Locate every Plasmodium parasite.
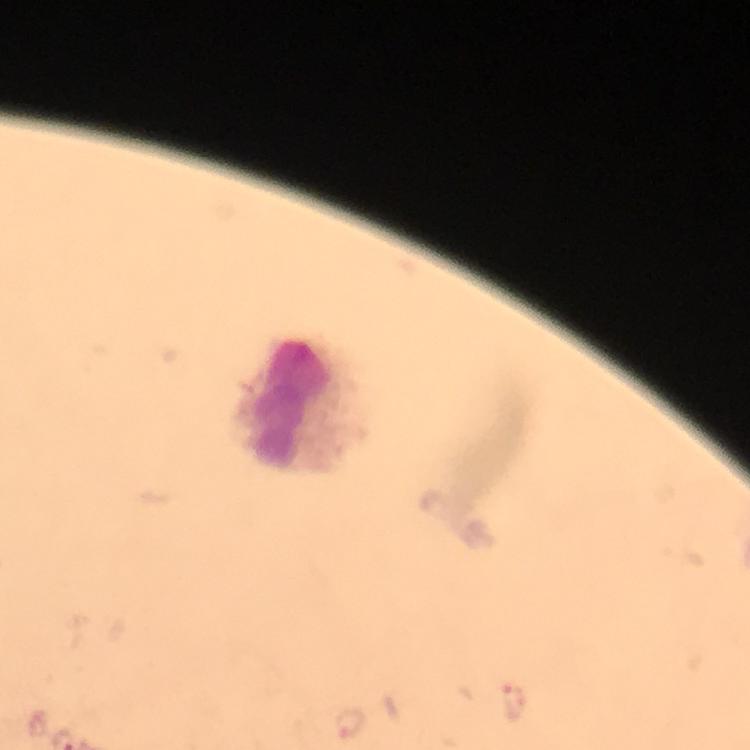
Approximate centers as {x, y} in pixels.
Plasmodium parasites: {514, 700}, {349, 723}.

Leukocyte locations: {303, 404}. At 100x magnification. Smartphone photograph taken through a microscope. Immersion oil was used. A crop from one field of view. Thick blood smear. From a diagnostic examination for malaria. Giemsa stain. Image is 750×750 pixels.